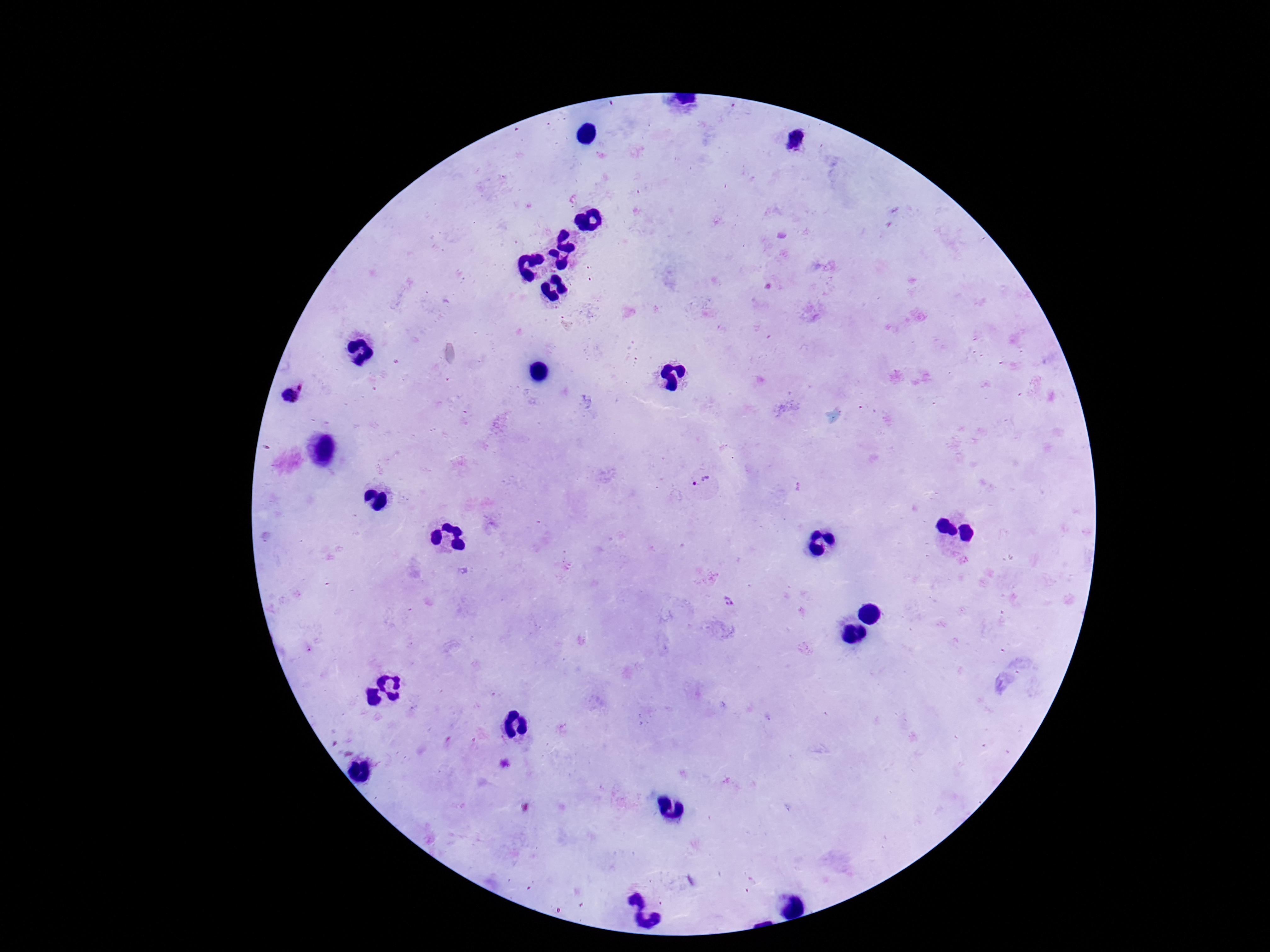
patient malaria status = infected
preparation = thick blood film
Plasmodium parasite locations = approximate centers as {x, y} in pixels: {291, 394}, {706, 483}, {728, 600}
image size = 1270×952 pixels
magnification = 100x
field of view = one from this slide
stain = Giemsa
capture = smartphone camera through the microscope eyepiece